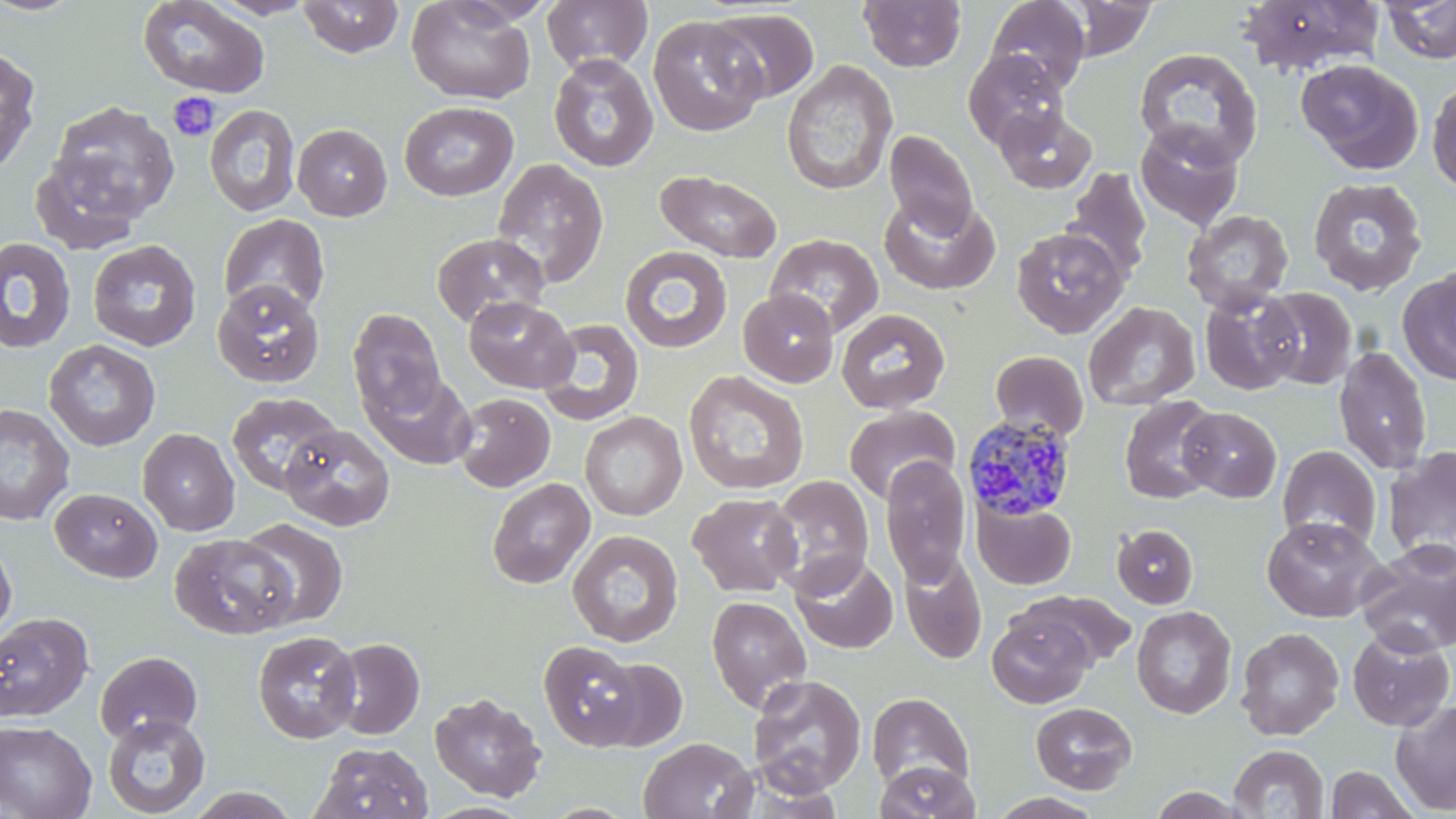
Summary:
  - Coordinate format: approximate bounding boxes as [x1, y1, x2, y2] in pixels
  - Plasmodium malariae-infected red blood cell locations: [963, 415, 1077, 522]
  - Uninfected red blood cell locations: [0, 0, 86, 16], [208, 0, 320, 19], [406, 0, 535, 104], [542, 0, 653, 74], [859, 0, 966, 73], [984, 0, 1090, 96], [1061, 0, 1158, 60], [1236, 0, 1384, 76], [1382, 0, 1456, 64], [137, 1, 270, 98], [298, 1, 404, 58], [708, 9, 819, 103], [647, 16, 766, 137], [0, 46, 41, 176], [1133, 48, 1263, 168], [963, 50, 1067, 150], [548, 54, 659, 173], [1296, 58, 1424, 175], [781, 60, 898, 196], [1427, 79, 1456, 195], [46, 99, 180, 226], [399, 100, 519, 201], [204, 104, 301, 217], [993, 105, 1095, 193], [1134, 122, 1244, 231], [293, 123, 392, 221], [885, 129, 979, 239], [28, 150, 149, 254], [492, 158, 609, 289], [1063, 167, 1153, 283], [655, 170, 783, 263], [1308, 176, 1427, 296], [879, 194, 1000, 295], [1181, 209, 1294, 315], [219, 213, 330, 318], [1011, 227, 1129, 339], [431, 233, 549, 328], [766, 234, 883, 338], [0, 236, 77, 355], [88, 239, 202, 352], [619, 245, 733, 353], [1398, 267, 1456, 385], [213, 278, 325, 387], [1257, 287, 1358, 390], [738, 289, 839, 387], [1199, 290, 1303, 396], [464, 296, 578, 393], [738, 297, 951, 392], [1083, 301, 1201, 410], [835, 307, 950, 414], [348, 308, 446, 420], [537, 318, 645, 426], [44, 339, 160, 451], [1334, 345, 1433, 474], [989, 351, 1089, 441], [683, 370, 810, 495], [365, 371, 476, 470], [227, 392, 342, 495], [453, 393, 555, 492], [1119, 396, 1222, 504], [0, 403, 75, 525], [843, 406, 960, 505], [1178, 407, 1282, 502], [580, 412, 687, 521], [280, 423, 395, 531], [137, 428, 240, 536], [1277, 444, 1382, 551], [1382, 445, 1456, 566], [880, 455, 972, 588], [766, 475, 875, 595], [487, 477, 595, 588], [50, 488, 162, 582], [688, 492, 802, 597], [972, 498, 1076, 589], [1261, 516, 1386, 622], [236, 518, 349, 629], [1111, 524, 1198, 609], [567, 529, 683, 648], [169, 533, 298, 639], [0, 536, 17, 641], [1357, 540, 1456, 656], [898, 550, 987, 664], [789, 553, 898, 654], [1017, 590, 1136, 671], [706, 595, 812, 714], [1131, 606, 1236, 719], [0, 613, 94, 722], [987, 614, 1092, 709], [1235, 627, 1344, 740], [1347, 627, 1454, 731], [252, 630, 361, 743], [328, 637, 425, 740], [538, 640, 644, 750], [95, 650, 202, 745], [595, 657, 688, 752], [747, 674, 867, 796], [429, 692, 546, 801], [867, 692, 974, 790], [1391, 699, 1456, 814], [1031, 701, 1137, 794], [102, 713, 211, 818], [0, 719, 96, 819], [638, 736, 757, 819], [312, 741, 432, 819], [1229, 744, 1328, 818], [873, 760, 981, 819], [1326, 765, 1420, 819], [185, 787, 302, 819], [988, 792, 1105, 818]
  - Platelet locations: [166, 93, 220, 143]
  - Slide-level diagnosis: Plasmodium malariae
  - Preparation: thin blood smear
  - Field of view: one of a larger specimen
  - Magnification: 1000x
  - Stain: May-Grünwald-Giemsa
  - Image size: 1456×819 pixels
  - Modality: optical microscopy